Name the parasite shown.
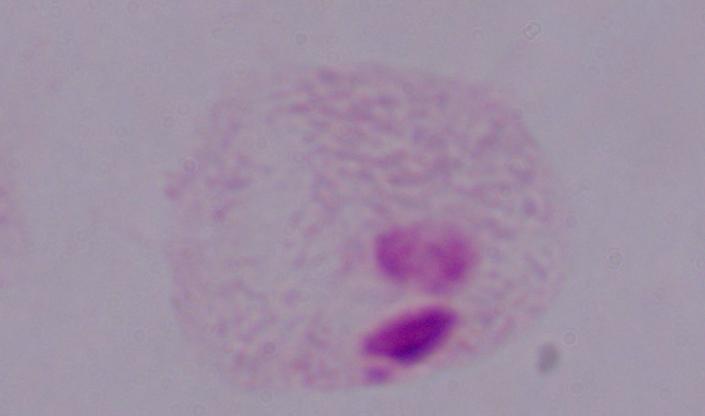

A trichomonad.

magnification = 1000x
modality = photomicrograph